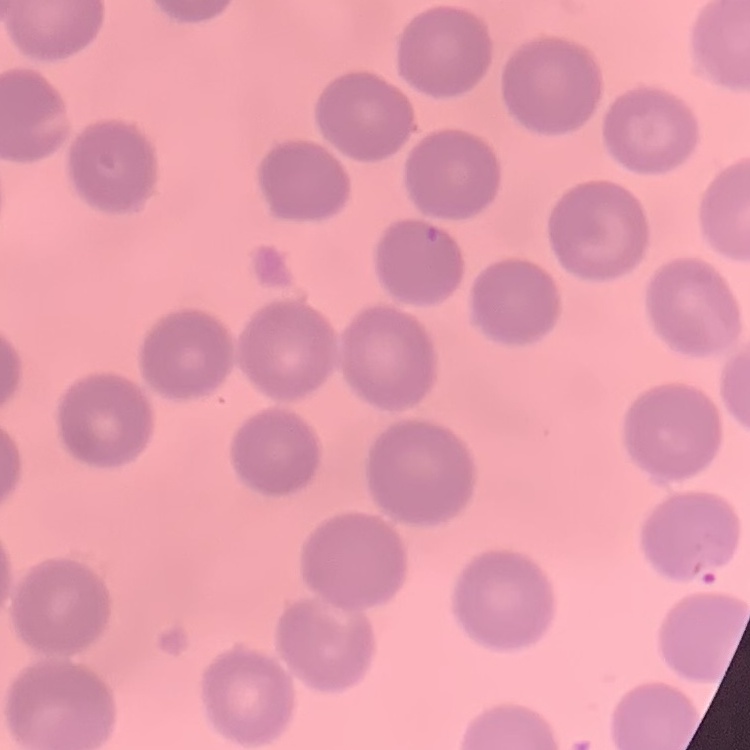
The red blood cells show no rouleaux formation. Square crop of a larger photomicrograph. Stained with either Field's or Giemsa. Thin peripheral smear.